Locate leukocytes (white blood cells).
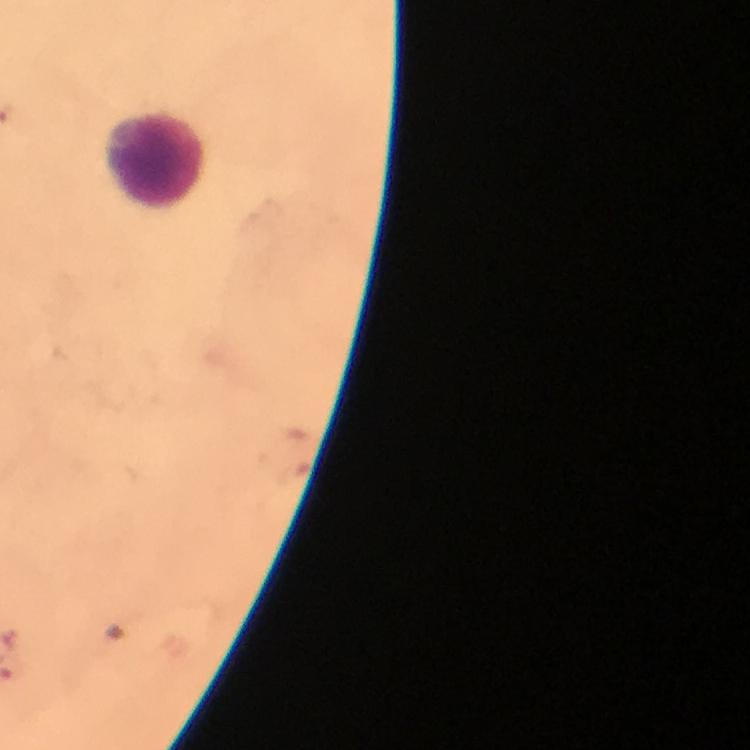
Approximate centers as (x, y) in pixels.
Leukocytes: (155, 165).

context = from a malaria diagnostic workup
immersion oil = applied
cropped from = a single field of view
preparation = thick smear
malaria parasites = none detected
image size = 750×750 pixels
capture = smartphone camera through the microscope
stain = Giemsa
magnification = 100x